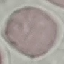
malaria status = uninfected
image type = cell patch, automatically extracted from a larger field of view and resized to 64 × 64 pixels
preparation = thin blood film
stain = Giemsa
capture = smartphone camera at the microscope eyepiece